Name the cell type shown.
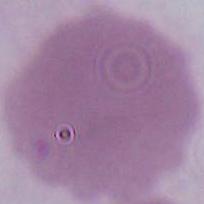

This is an erythrocyte.

Summary:
  - Magnification: 1000x
  - Modality: photomicrograph